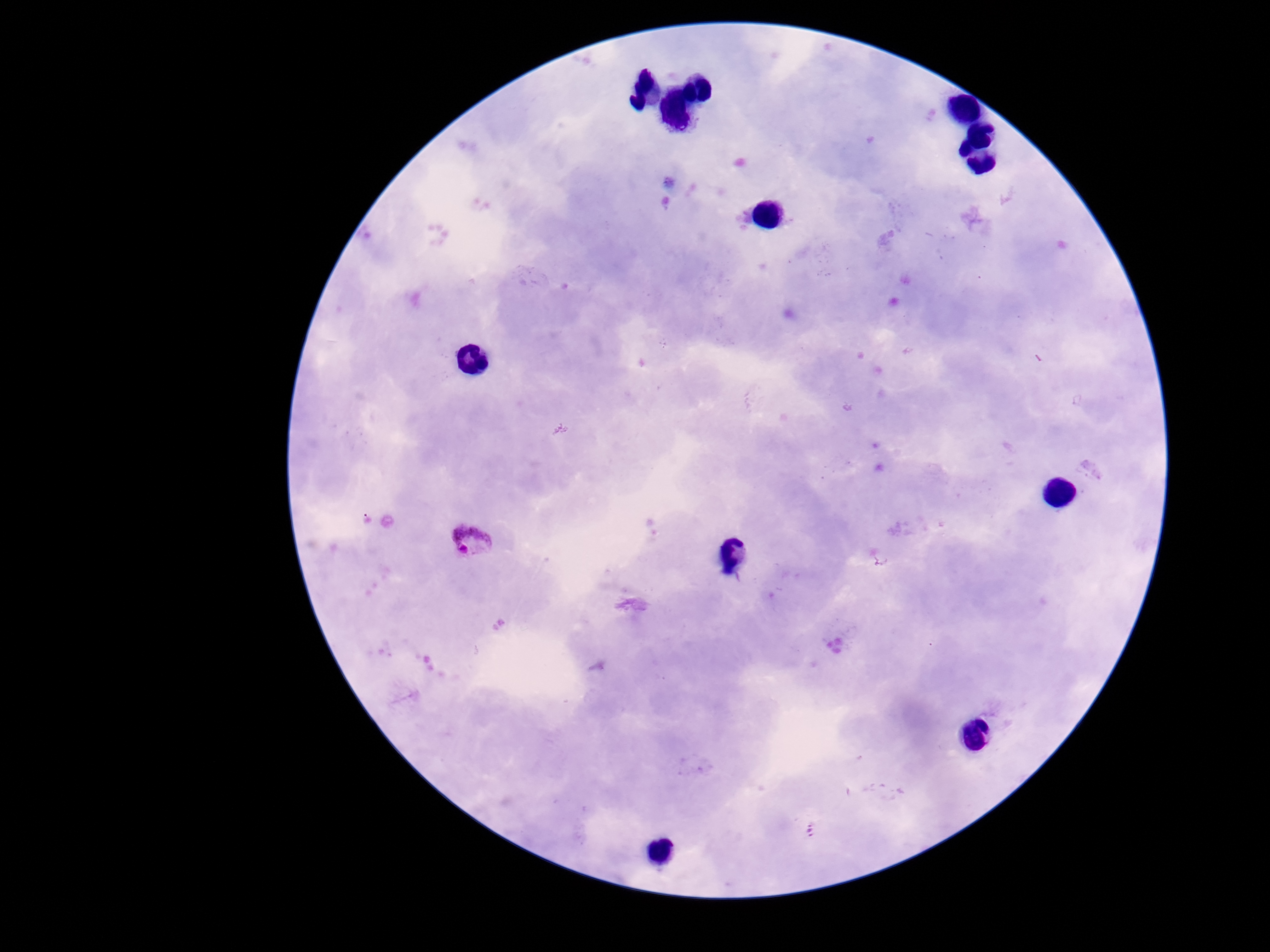
Approximate object centers, in pixels from the top-left corner.
Summary:
  - Plasmodium parasite locations: (x=471, y=539)
  - Capture: smartphone camera through the microscope eyepiece
  - Stain: Giemsa
  - Patient malaria status: infected
  - Image size: 1270×952 pixels
  - Preparation: thick peripheral-blood smear
  - Field of view: single
  - Magnification: 100x